Report the malaria status of this cell.
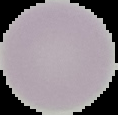

It is uninfected.

image type = segmented cell region with the area outside set to black
preparation = thin blood film
image size = 118×115 pixels